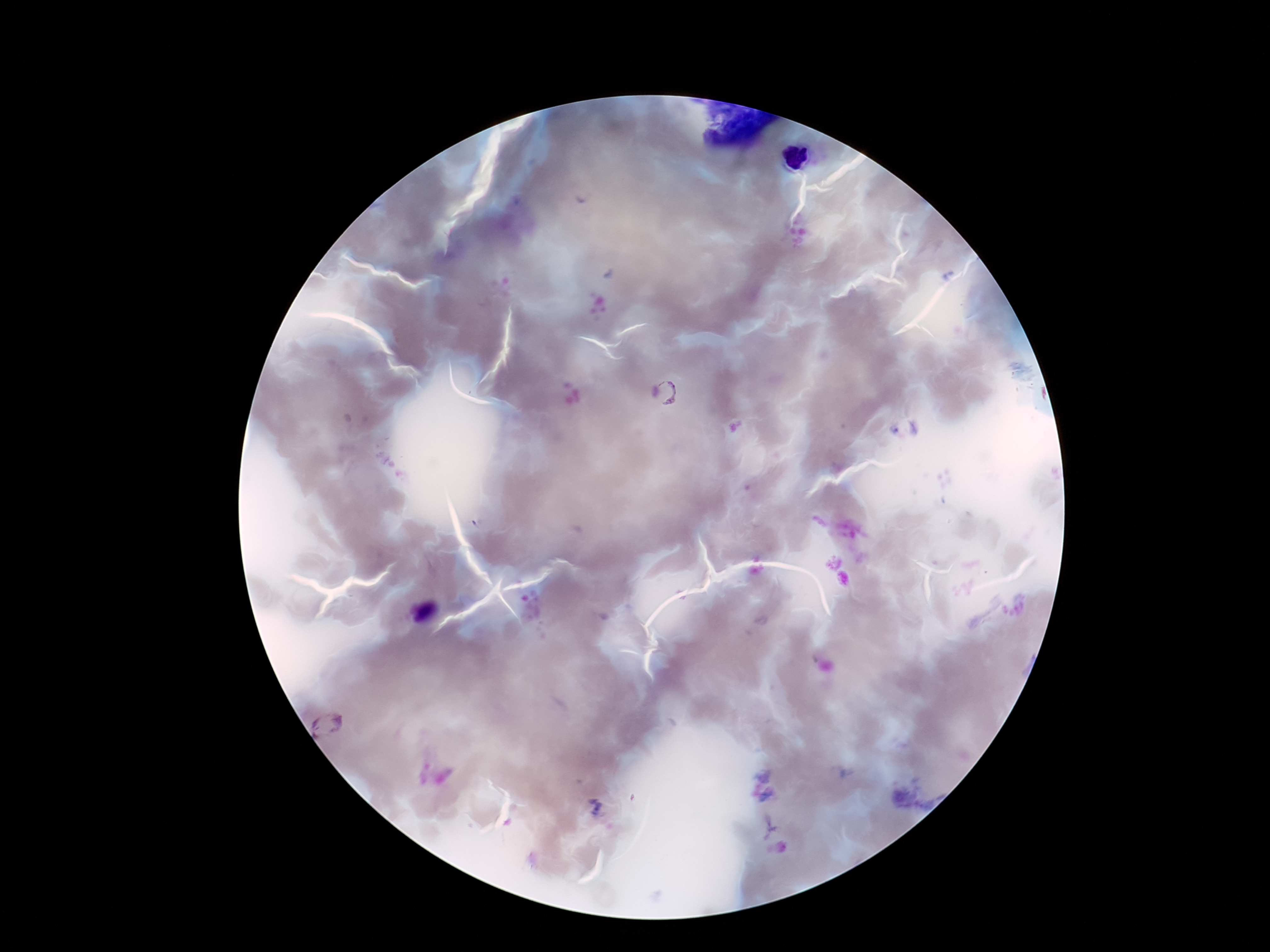

magnification = 100x
stain = Giemsa
preparation = thick blood film
capture = smartphone camera through the microscope eyepiece
patient malaria status = positive
image size = 1270×952 pixels
Plasmodium parasite locations = approximate centers as (x, y) in pixels: (674, 393), (334, 725)
field of view = single